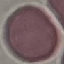

result = no malaria parasites detected
image type = automatically extracted cell patch, resized to 64 × 64 pixels
capture = smartphone camera at the microscope eyepiece
stain = Giemsa
preparation = thin blood film